Outline platelets.
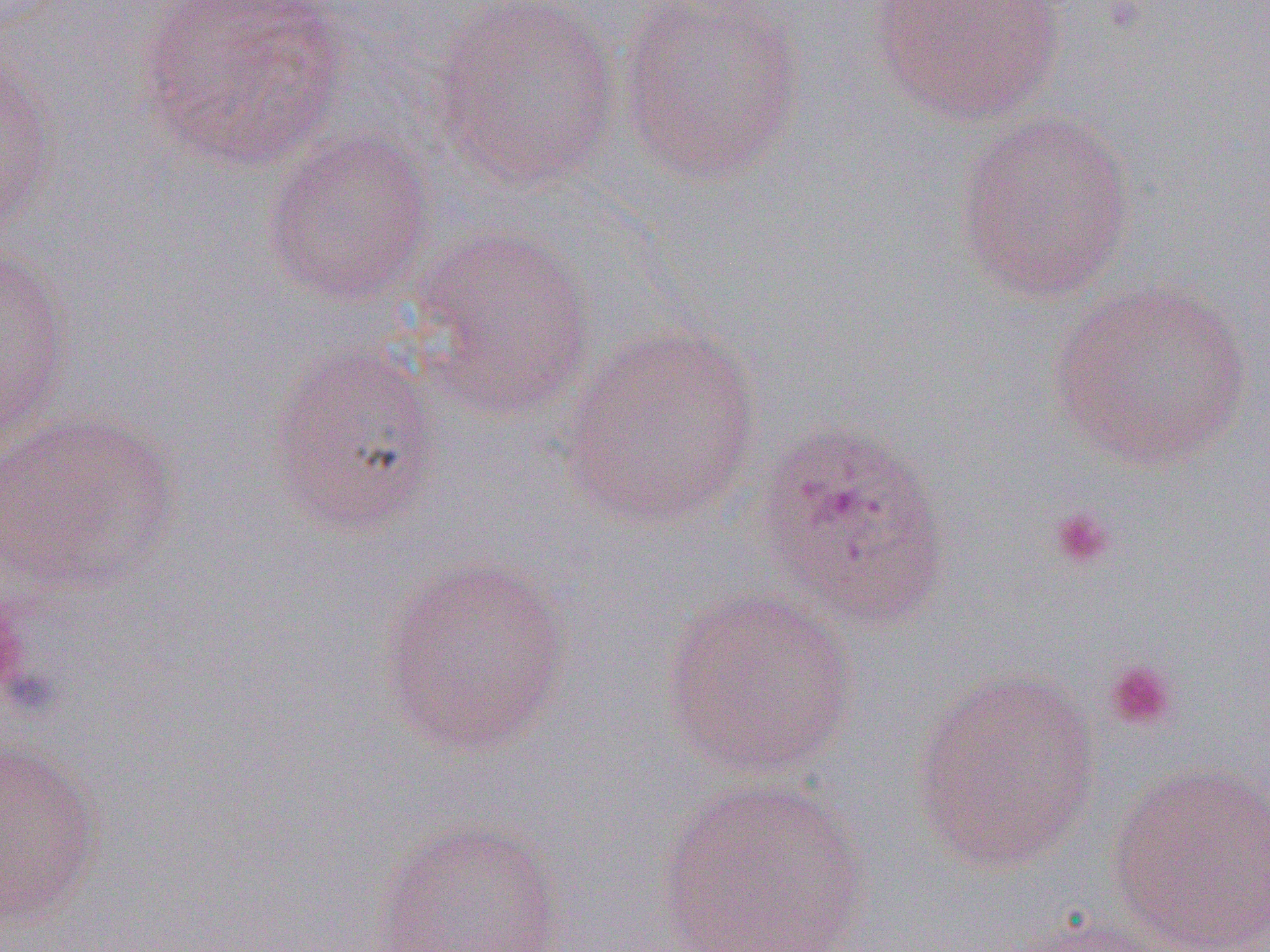
Approximate bounding boxes as [x1, y1, x2, y2] in pixels.
Platelets: [1048, 505, 1119, 572], [1101, 658, 1180, 733].

Uninfected red blood cell locations (subset): [134, 0, 352, 172], [427, 0, 623, 191], [616, 0, 807, 185], [870, 0, 1069, 127], [1, 53, 58, 240], [953, 111, 1137, 302], [263, 127, 435, 305], [409, 225, 598, 422], [1, 245, 74, 445], [1046, 280, 1255, 472], [556, 323, 763, 531], [267, 341, 444, 536], [1, 411, 180, 595], [377, 556, 573, 756], [660, 586, 859, 779], [909, 669, 1102, 876], [0, 740, 102, 923], [1105, 763, 1270, 951], [656, 776, 872, 952], [371, 818, 568, 952], [1002, 914, 1184, 952]. Slide-level diagnosis: Plasmodium ovale. Light microscopy. Thin blood smear. One field of a larger specimen. 1000x magnification. Image is 1270×952 pixels.